State which parasite is depicted.
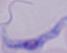
A trypanosome.

Photomicrograph. 1000x magnification.